State which parasite is depicted.
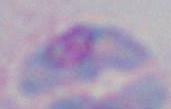
Toxoplasma gondii.

Summary:
  - Modality: micrograph
  - Magnification: 1000x